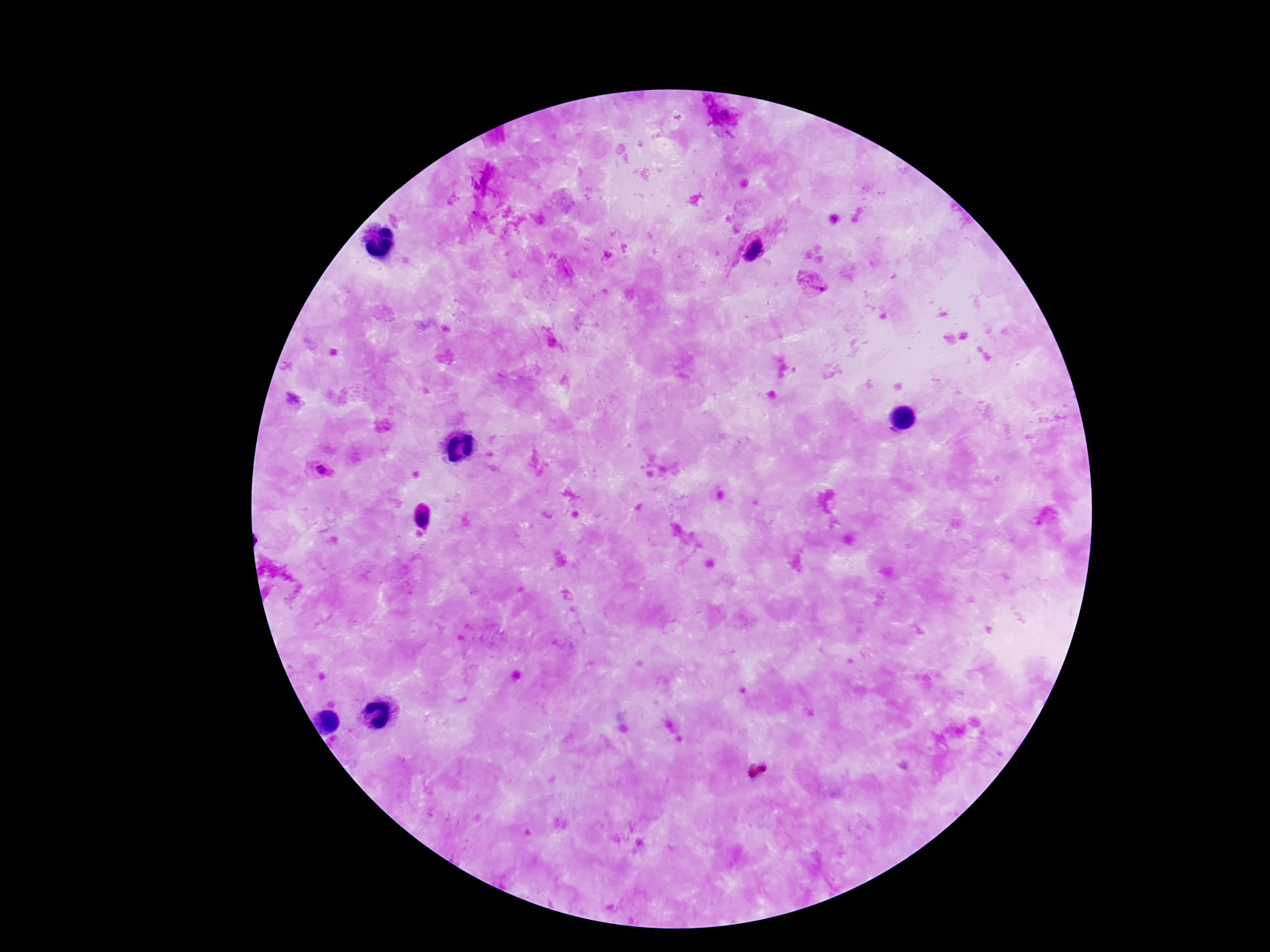

Approximate centers as (x, y) in pixels. Plasmodium parasite locations: (723, 117), (754, 252), (814, 285), (323, 472), (423, 519). Thick peripheral-blood smear. Giemsa-stained preparation. Image is 1270×952 pixels. 100x magnification. Single field of view. Patient malaria status: infected. Smartphone photograph taken through the microscope eyepiece.